Report the malaria status of this cell.
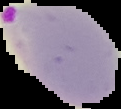
Parasitized.

Segmented cell region on a black background. Image is 121×109 pixels. From a thin blood film.